Assess the morphology of the erythrocytes.
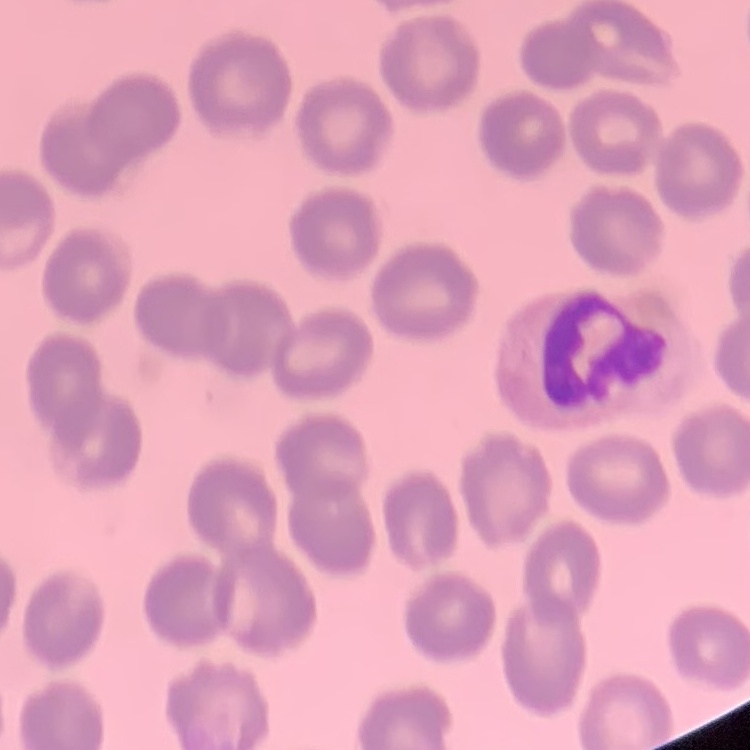
No rouleaux formation.

image type = one tile cut from a larger photomicrograph
stain = Field's or Giemsa
preparation = thin blood film